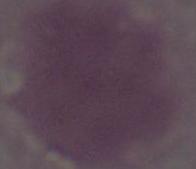
Summary:
  - Identification: erythrocyte
  - Magnification: 1000x
  - Modality: photomicrograph